Identify the parasite.
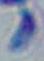
Toxoplasma gondii.

Summary:
  - Modality: photomicrograph
  - Magnification: 1000x